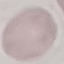 Malaria status: uninfected. Cell patch, automatically extracted from a larger field of view and resized to 64 × 64 pixels. Thin blood smear. Giemsa-stained preparation. Acquired by smartphone through the microscope eyepiece.